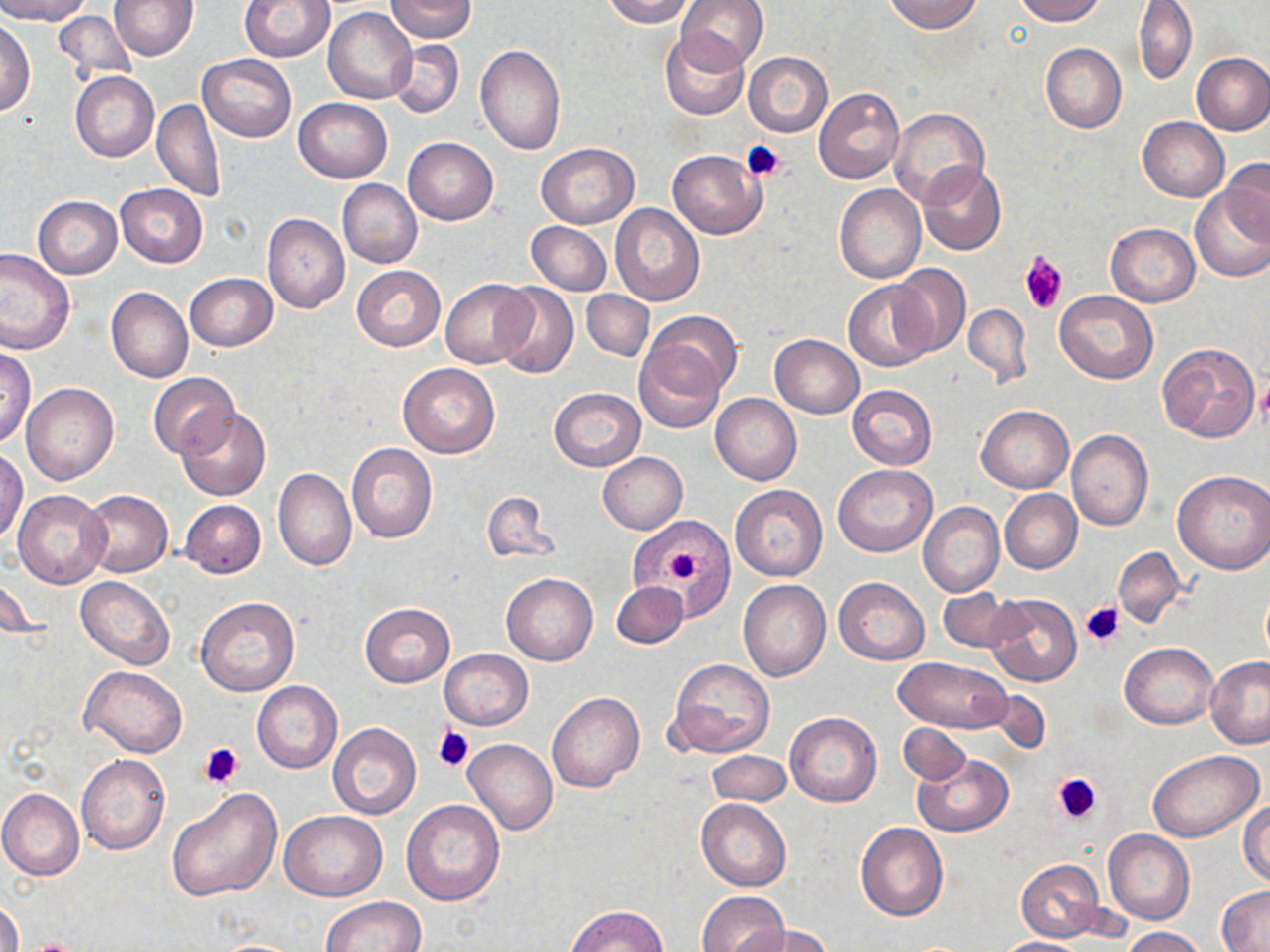 Approximate bounding boxes as (x1, y1, x2, y2) in pixels. Platelet locations: (742, 140, 787, 181), (1020, 251, 1066, 314), (1255, 380, 1270, 425), (654, 531, 713, 596), (1083, 601, 1127, 649), (432, 726, 474, 772), (198, 742, 244, 789), (1052, 771, 1104, 826), (24, 940, 83, 952). Uninfected red blood cell locations: (0, 0, 92, 24), (109, 0, 197, 60), (239, 0, 335, 62), (385, 0, 477, 42), (599, 0, 695, 27), (677, 0, 769, 74), (883, 0, 982, 34), (1010, 0, 1106, 25), (1133, 0, 1197, 84), (324, 7, 417, 104), (54, 11, 138, 84), (0, 18, 35, 116), (660, 29, 751, 120), (388, 39, 465, 119), (1040, 43, 1127, 132), (474, 44, 566, 155), (743, 52, 833, 137), (1191, 52, 1270, 135), (197, 55, 297, 143), (70, 71, 159, 161), (814, 88, 905, 184), (293, 97, 393, 182), (152, 98, 225, 202), (889, 108, 989, 206), (1137, 117, 1229, 202), (403, 137, 498, 225), (537, 143, 638, 228), (667, 149, 766, 238), (1222, 158, 1269, 242), (917, 161, 1005, 255), (337, 179, 423, 268), (834, 183, 925, 283), (115, 184, 208, 268), (1189, 187, 1270, 282), (33, 195, 122, 279), (609, 204, 706, 308), (262, 213, 350, 313), (526, 221, 611, 296), (1105, 223, 1199, 306), (0, 247, 75, 356), (887, 264, 971, 358), (352, 265, 446, 351), (185, 273, 277, 351), (441, 278, 535, 368), (844, 280, 937, 372), (491, 282, 580, 380), (106, 287, 193, 384), (582, 289, 654, 360), (1054, 291, 1159, 384), (961, 304, 1031, 388), (642, 311, 742, 398), (770, 334, 865, 418), (634, 339, 724, 431), (1155, 340, 1262, 444), (0, 346, 36, 448), (397, 362, 501, 457), (147, 372, 241, 461), (21, 382, 118, 485), (847, 385, 937, 469), (548, 388, 645, 471), (710, 393, 802, 486), (977, 405, 1073, 493), (176, 407, 271, 501), (1066, 429, 1153, 531), (346, 444, 437, 543), (1, 448, 28, 546), (597, 452, 687, 534), (832, 463, 937, 557), (273, 467, 357, 570), (1172, 469, 1270, 574), (730, 485, 827, 581), (1000, 489, 1082, 574), (13, 490, 109, 589), (80, 490, 172, 576), (481, 490, 558, 565), (178, 499, 267, 578), (918, 502, 1003, 597), (636, 522, 732, 609), (1113, 546, 1187, 627), (1, 566, 43, 645), (501, 573, 598, 666), (75, 575, 174, 670), (834, 577, 929, 664), (738, 579, 831, 682), (611, 580, 689, 649), (936, 588, 1021, 654), (982, 592, 1081, 687), (196, 596, 299, 697), (360, 603, 454, 687), (1120, 643, 1218, 728), (438, 649, 533, 729), (894, 657, 1013, 733), (1205, 657, 1270, 749), (667, 658, 775, 758), (81, 664, 188, 757), (252, 681, 342, 772), (547, 692, 644, 793), (784, 712, 882, 806), (328, 722, 421, 820), (899, 723, 972, 785), (463, 740, 558, 834), (707, 750, 791, 806), (1146, 750, 1264, 841), (76, 754, 169, 855), (913, 754, 1013, 836), (1, 788, 84, 879), (167, 788, 282, 903), (400, 799, 505, 905), (696, 799, 790, 891), (1239, 799, 1269, 886), (279, 811, 388, 901), (856, 822, 947, 922), (1103, 831, 1194, 924), (1016, 859, 1104, 942), (1218, 885, 1270, 950), (696, 890, 787, 952), (1, 897, 23, 952), (320, 897, 428, 952), (565, 905, 667, 952), (741, 924, 836, 952), (1121, 926, 1209, 952), (993, 937, 1087, 952). Slide-level diagnosis: negative for blood parasites. May-Grünwald-Giemsa stain. One field of a larger specimen. Light microscopy. 1000x magnification. Image is 1270×952 pixels. Thin blood film.